Describe the morphology of the erythrocytes.
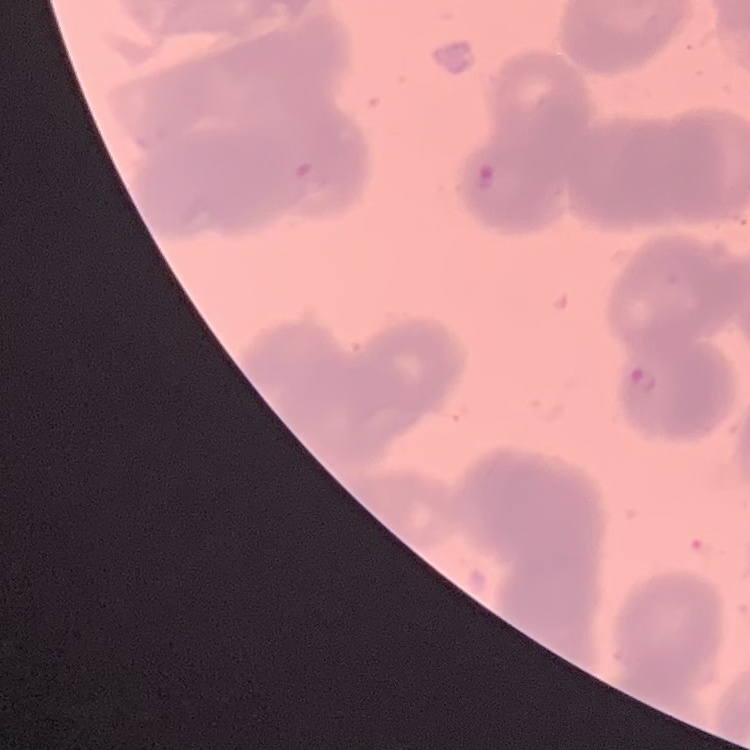
They show rouleaux formation.

Summary:
  - Preparation: thin peripheral smear
  - Image type: square crop of a larger photomicrograph
  - Stain: Field's or Giemsa